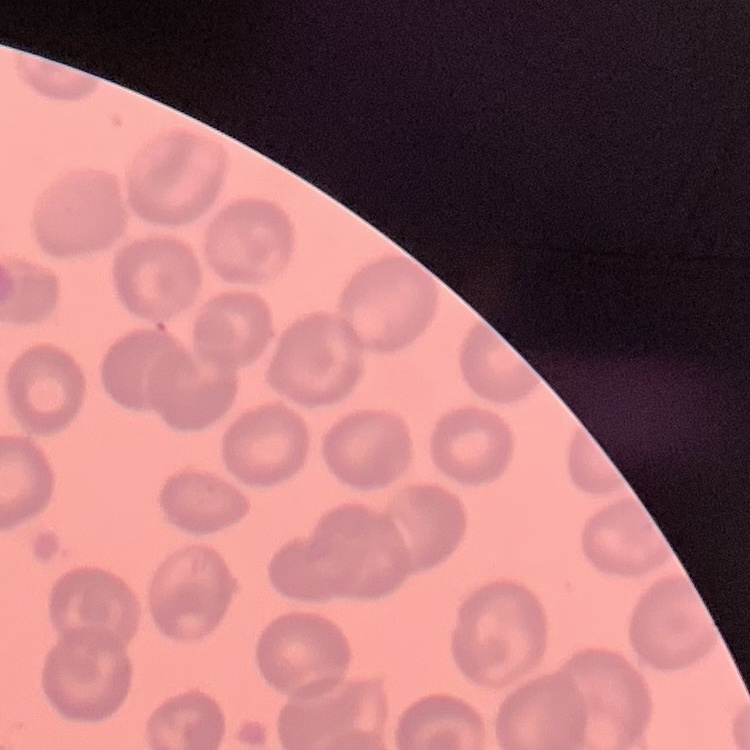 The red blood cells show no rouleaux formation. Field's or Giemsa stain. One tile cut from a larger photomicrograph. Thin blood smear.